Report the malaria status of this cell.
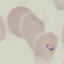
It is parasitized.

Photographed with a smartphone camera at the microscope eyepiece. Cell patch, automatically extracted from a larger field of view and resized to 64 × 64 pixels. Giemsa-stained preparation. Thin blood smear.